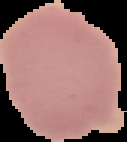

The area outside the segmented cell region is set to black. From a thin blood smear. Image is 127×142 pixels. Malaria status: uninfected.